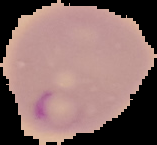
From a thin blood smear. Segmented cell region on a black background. Malaria status: parasitized. Image is 157×145 pixels.